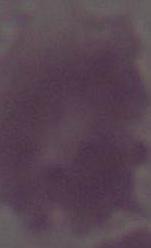

Summary:
  - Magnification: 1000x
  - Identification: red blood cell
  - Modality: photomicrograph